Assess this cell for malaria.
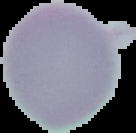

It is uninfected.

Summary:
  - Image size: 136×133 pixels
  - Preparation: thin blood smear
  - Image type: segmented cell region with the area outside set to black